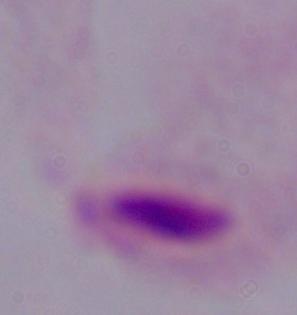

identification: trichomonad
magnification: 1000x
modality: micrograph